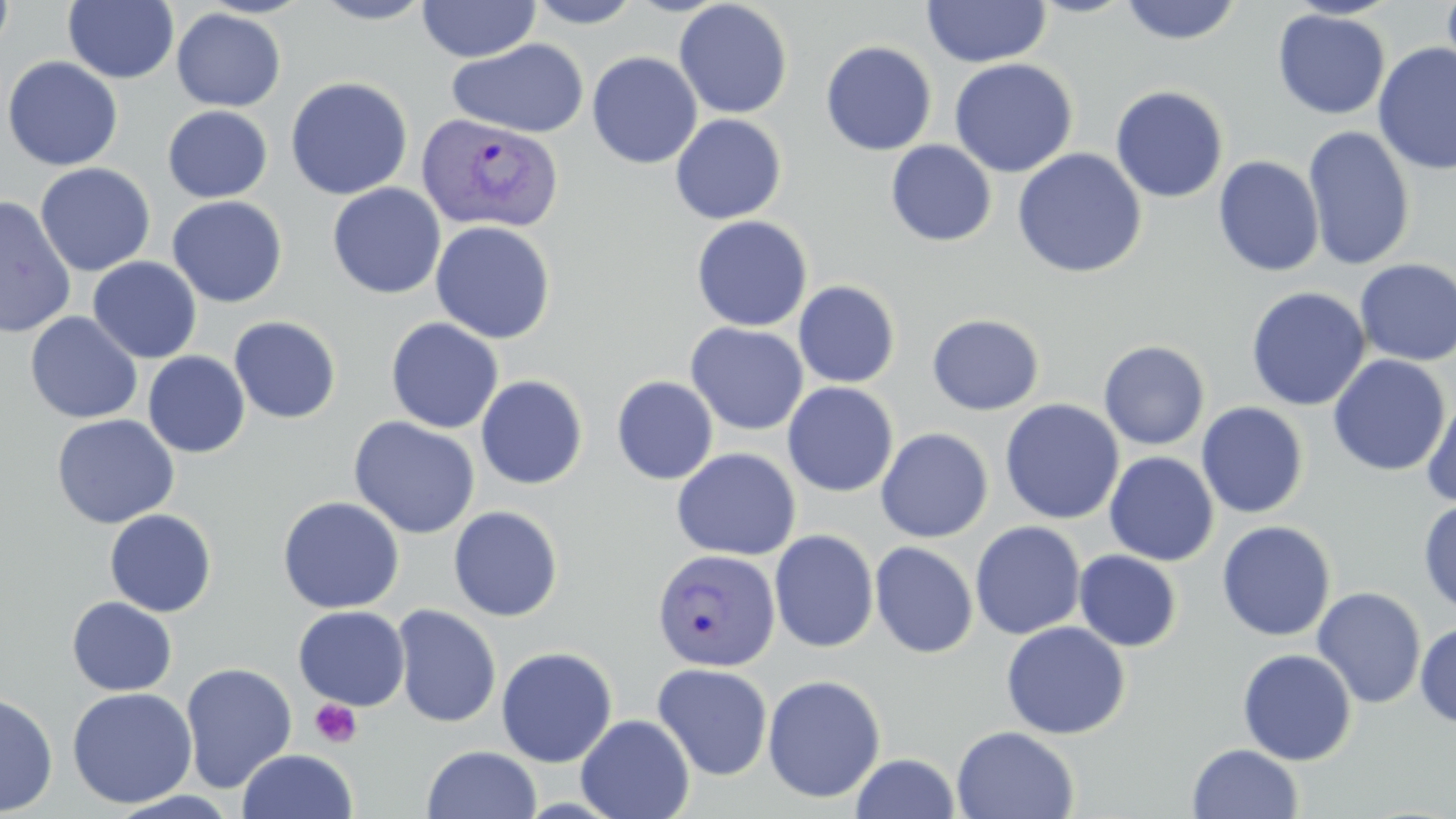

slide-level diagnosis = Plasmodium vivax
magnification = 1000x
image size = 1456×819 pixels
uninfected red blood cell locations = approximate bounding boxes as (x1, y1, x2, y2) in pixels: (0, 0, 16, 59), (63, 0, 179, 84), (311, 0, 436, 25), (524, 0, 644, 28), (922, 0, 1051, 68), (1118, 0, 1243, 45), (1441, 0, 1456, 79), (416, 1, 541, 62), (673, 1, 793, 119), (171, 7, 287, 111), (1273, 9, 1390, 119), (447, 39, 589, 138), (820, 41, 937, 156), (1372, 42, 1456, 176), (587, 51, 702, 169), (1, 56, 123, 171), (949, 58, 1079, 178), (285, 77, 413, 200), (1110, 85, 1229, 203), (162, 105, 273, 202), (670, 113, 787, 224), (1302, 125, 1416, 270), (885, 140, 997, 247), (1012, 148, 1147, 279), (1213, 155, 1325, 277), (35, 162, 156, 276), (327, 182, 446, 299), (0, 195, 76, 338), (166, 196, 288, 308), (690, 215, 813, 332), (430, 221, 556, 343), (87, 256, 202, 364), (1355, 259, 1456, 367), (793, 280, 901, 388), (1246, 287, 1371, 411), (25, 311, 143, 424), (927, 313, 1045, 415), (228, 316, 342, 423), (384, 317, 504, 434), (685, 322, 808, 436), (1098, 340, 1210, 450), (142, 351, 250, 458), (1327, 354, 1451, 477), (475, 375, 588, 490), (611, 376, 718, 485), (782, 382, 899, 497), (1420, 391, 1456, 509), (999, 399, 1124, 525), (1196, 402, 1309, 519), (51, 414, 179, 529), (348, 416, 481, 540), (875, 428, 993, 542), (671, 447, 801, 561), (1104, 451, 1219, 566), (277, 496, 405, 614), (1418, 498, 1456, 617), (447, 505, 564, 622), (104, 508, 217, 617), (1216, 520, 1336, 642), (970, 521, 1086, 640), (769, 529, 879, 653), (869, 541, 979, 659), (1074, 550, 1182, 652), (1312, 587, 1426, 709), (66, 596, 178, 696), (293, 605, 409, 710), (391, 605, 502, 727), (1001, 621, 1130, 740), (1415, 622, 1456, 728), (496, 646, 618, 767), (1237, 648, 1357, 766), (180, 661, 298, 794), (652, 662, 773, 780), (762, 674, 886, 803), (66, 687, 197, 809), (0, 691, 58, 816), (576, 714, 695, 819), (951, 726, 1080, 818), (1187, 743, 1303, 818), (422, 745, 541, 819), (238, 749, 357, 819), (850, 753, 962, 818)
modality = optical microscopy
stain = May-Grünwald-Giemsa
field of view = one of a larger specimen
Plasmodium vivax-infected red blood cell locations = approximate bounding boxes as (x1, y1, x2, y2) in pixels: (417, 112, 563, 234), (651, 548, 781, 671)
preparation = thin blood smear
platelet locations = approximate bounding boxes as (x1, y1, x2, y2) in pixels: (310, 698, 363, 747)